Point out Plasmodium parasites and leukocytes.
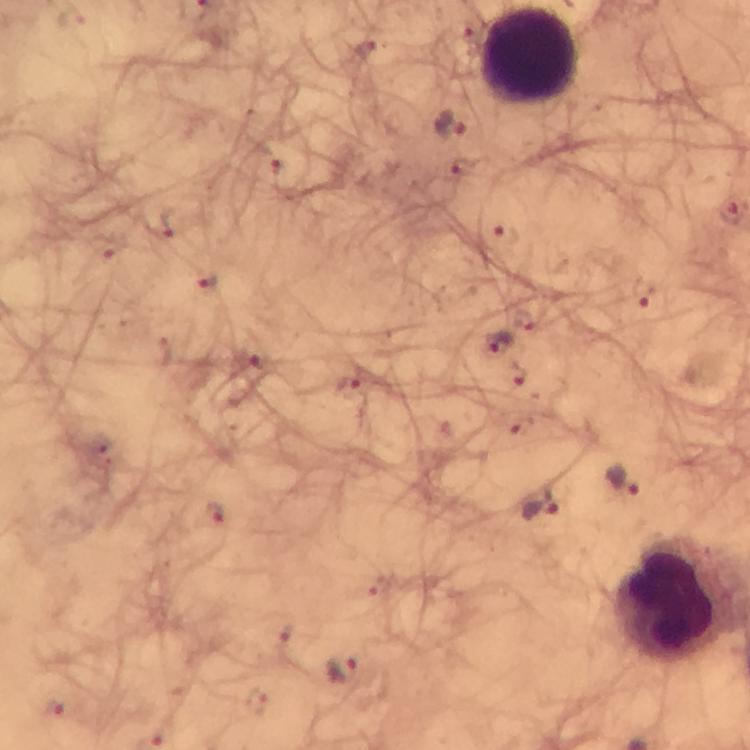

Approximate centers as [x, y] in pixels.
Plasmodium parasites: [451, 124], [498, 344], [624, 482], [539, 503], [343, 670].
Leukocytes: [529, 56], [676, 600].

preparation: thick blood film
image_size: 750×750 pixels
cropped_from: a single field of view
context: from a malaria diagnostic workup
stain: Giemsa
magnification: 100x
capture: smartphone mounted on the microscope
immersion_oil: used